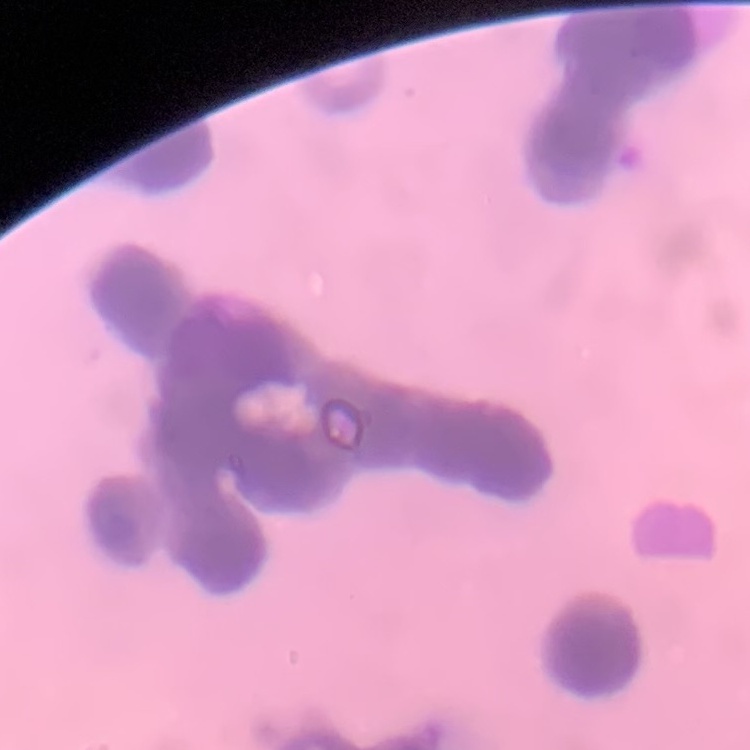
The red blood cells show rouleaux formation. Thin blood film. Stained with either Field's or Giemsa. Square crop of a larger photomicrograph.